Give the extent of all Plasmodium vivax-infected red blood cells.
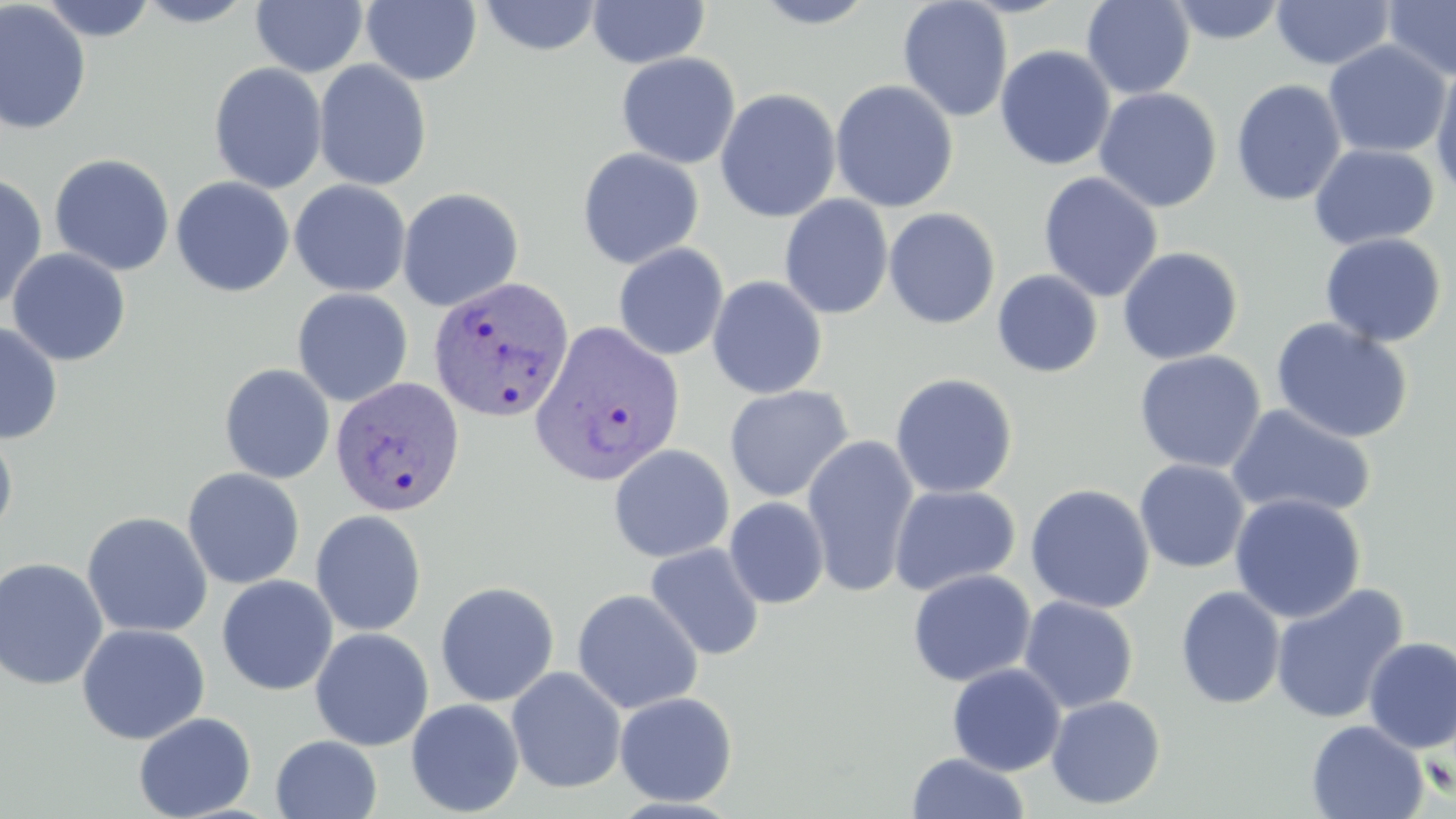

Approximate bounding boxes as [x1, y1, x2, y2] in pixels.
Plasmodium vivax-infected red blood cells: [428, 276, 575, 424], [530, 319, 687, 487], [330, 376, 465, 518].

slide_level_diagnosis: Plasmodium vivax
preparation: thin blood smear
stain: May-Grünwald-Giemsa
magnification: 1000x
modality: light microscopy
field_of_view: single
image_size: 1456×819 pixels
uninfected_red_blood_cell_locations: 'approximate bounding boxes as [x1, y1, x2, y2] in pixels: [37, 0, 159, 42], [132, 0, 260, 27], [251, 0, 368, 77], [478, 0, 603, 57], [587, 0, 710, 69], [749, 0, 882, 29], [897, 0, 1014, 123], [1081, 0, 1196, 100], [0, 1, 93, 136], [361, 1, 482, 86], [1166, 1, 1288, 45], [1271, 1, 1396, 70], [1383, 1, 1456, 83], [1286, 9, 1424, 123], [1323, 40, 1451, 159], [994, 45, 1116, 171], [615, 52, 741, 169], [313, 60, 433, 191], [1430, 61, 1456, 200], [208, 62, 328, 194], [830, 79, 959, 213], [1231, 79, 1347, 207], [1094, 87, 1223, 212], [715, 88, 841, 223], [1308, 143, 1440, 251], [577, 147, 704, 269], [48, 153, 175, 276], [1037, 171, 1164, 303], [0, 172, 48, 312], [171, 176, 294, 298], [289, 179, 412, 297], [397, 187, 524, 311], [779, 195, 894, 319], [883, 207, 1001, 329], [1320, 232, 1447, 348], [612, 242, 729, 361], [1117, 246, 1244, 365], [6, 248, 131, 366], [992, 269, 1103, 378], [707, 275, 828, 399], [292, 288, 413, 407], [1271, 317, 1414, 443], [0, 319, 63, 445], [1133, 349, 1267, 473], [219, 363, 335, 484], [889, 372, 1018, 499], [724, 385, 853, 503], [1226, 404, 1377, 521], [0, 423, 18, 542], [802, 435, 920, 598], [608, 443, 734, 562], [1134, 459, 1250, 573], [182, 467, 305, 589], [1025, 483, 1155, 614], [888, 484, 1021, 596], [1229, 493, 1366, 623], [724, 497, 830, 609], [310, 510, 427, 637], [82, 511, 213, 638], [644, 543, 765, 661], [0, 557, 108, 691], [907, 569, 1036, 687], [216, 574, 338, 696], [435, 581, 559, 707], [1270, 583, 1409, 725], [1175, 586, 1286, 709], [571, 587, 703, 714], [1018, 596, 1139, 712], [76, 623, 211, 744], [309, 627, 434, 751], [1362, 637, 1456, 754], [947, 663, 1066, 776], [506, 666, 627, 794], [614, 691, 738, 807], [1045, 695, 1166, 810], [405, 698, 524, 817], [133, 712, 257, 819], [1305, 719, 1429, 819], [270, 735, 383, 819], [906, 752, 1029, 819]'